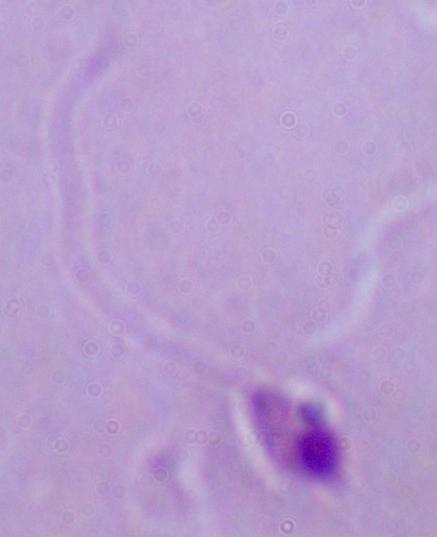
identification = Leishmania
magnification = 1000x
modality = micrograph